Report the malaria status of this cell.
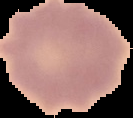
It is uninfected.

From a thin blood film. Image is 133×118 pixels. Segmented cell region on a black background.